Identify the preparation type.
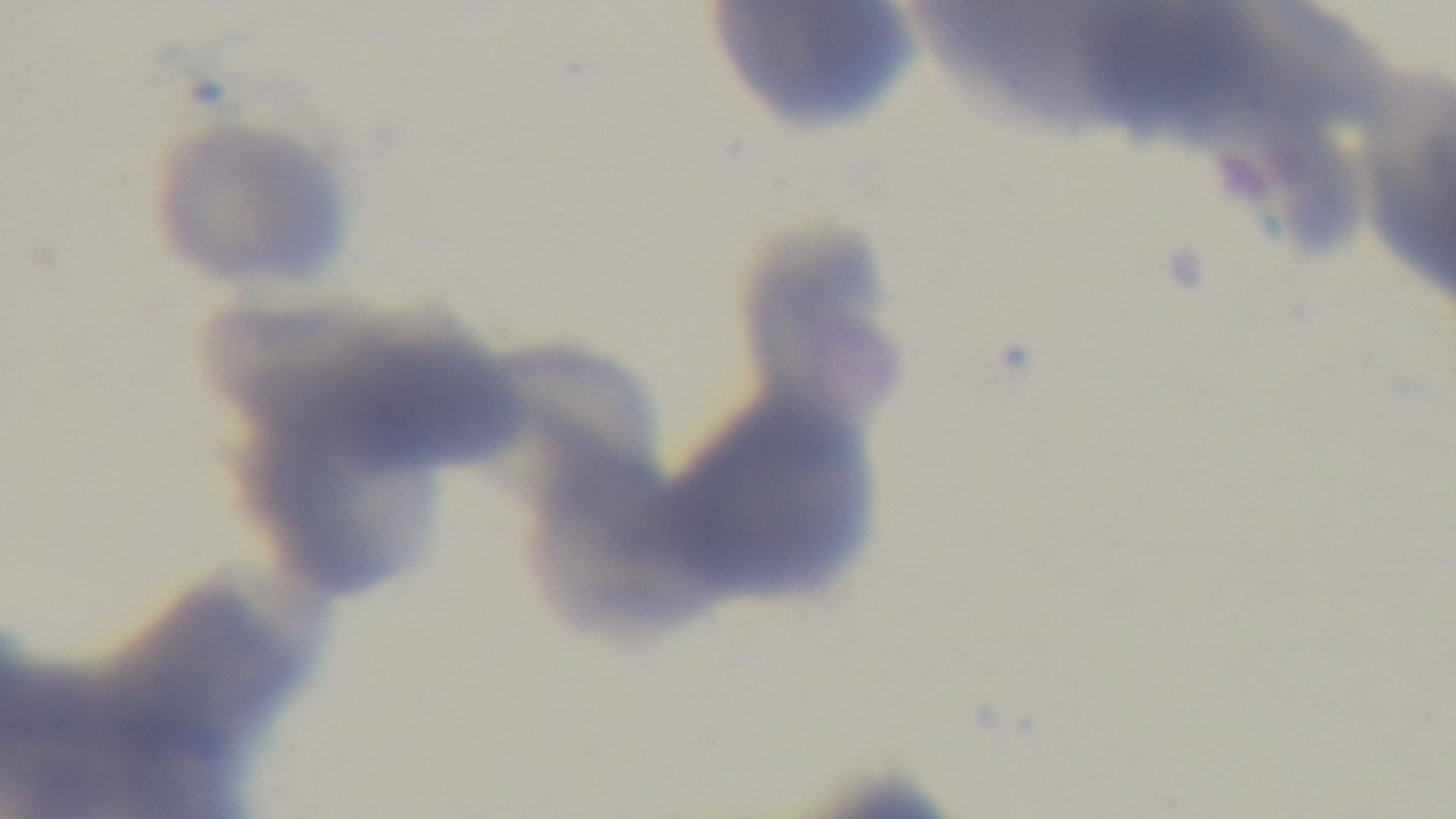
Thin.

Giemsa stain. Light microscopy. Captured with a mounted 4K digital camera. 100x oil-immersion objective. Malaria status: negative. Single field of view.